Describe the morphology of the red blood cells.
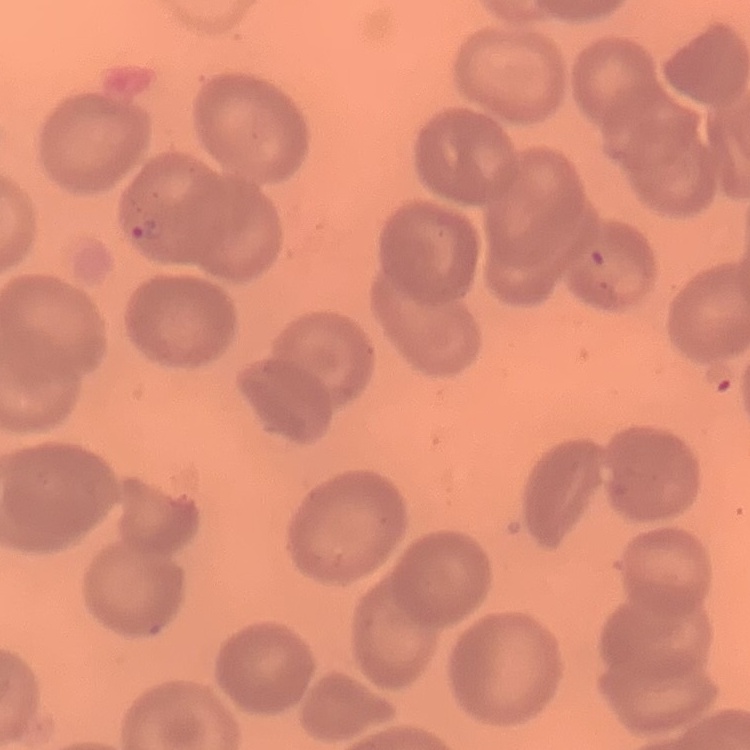

No rouleaux formation.

{
  "preparation": "thin peripheral smear",
  "image_type": "one tile cut from a larger photomicrograph",
  "stain": "Field's or Giemsa"
}